Assess the morphology of the erythrocytes.
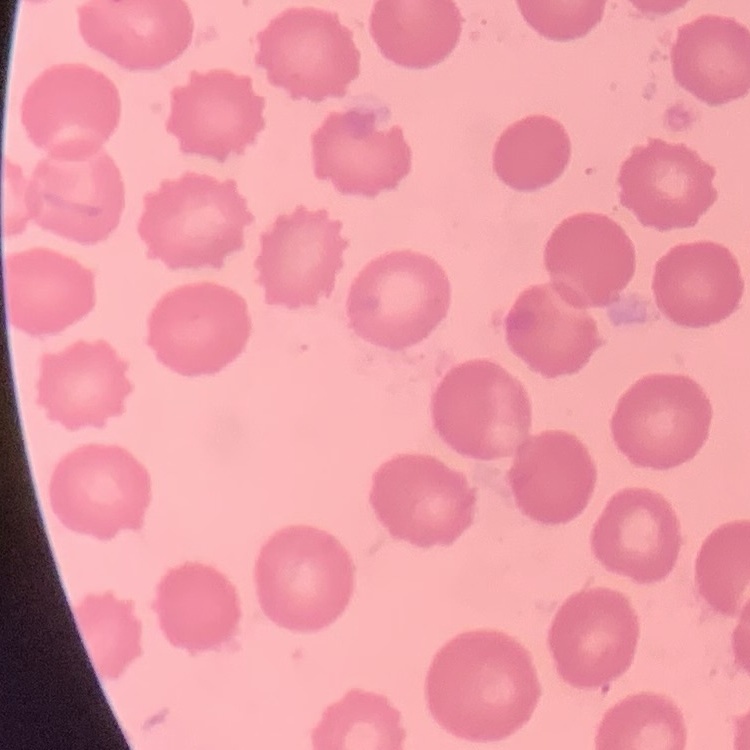
They show no rouleaux formation.

Summary:
  - Image type: one tile cut from a larger photomicrograph
  - Stain: Field's or Giemsa
  - Preparation: thin peripheral smear